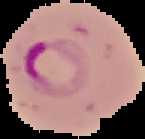

Summary:
  - Image size: 145×139 pixels
  - Image type: segmented cell region on a black background
  - Preparation: thin blood smear
  - Malaria status: parasitized